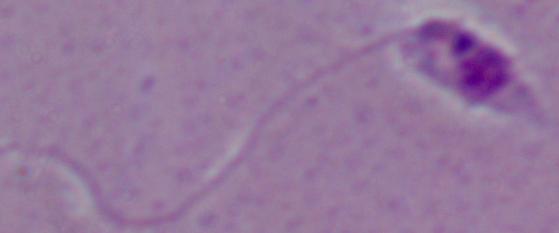
Summary:
  - Magnification: 1000x
  - Identification: Leishmania
  - Modality: micrograph